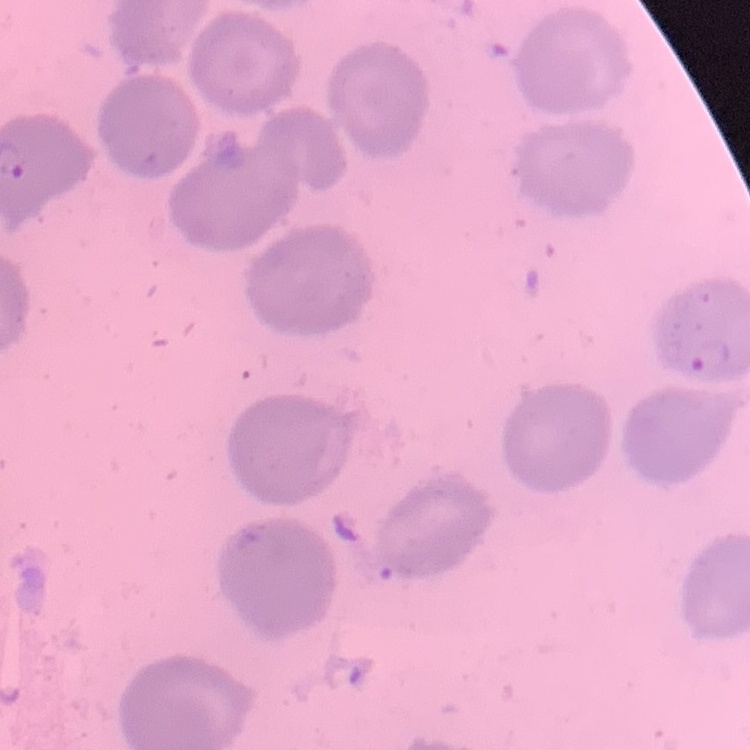

Summary:
  - Erythrocyte morphology: no rouleaux formation
  - Stain: Field's or Giemsa
  - Preparation: thin blood smear
  - Image type: one tile cut from a larger photomicrograph